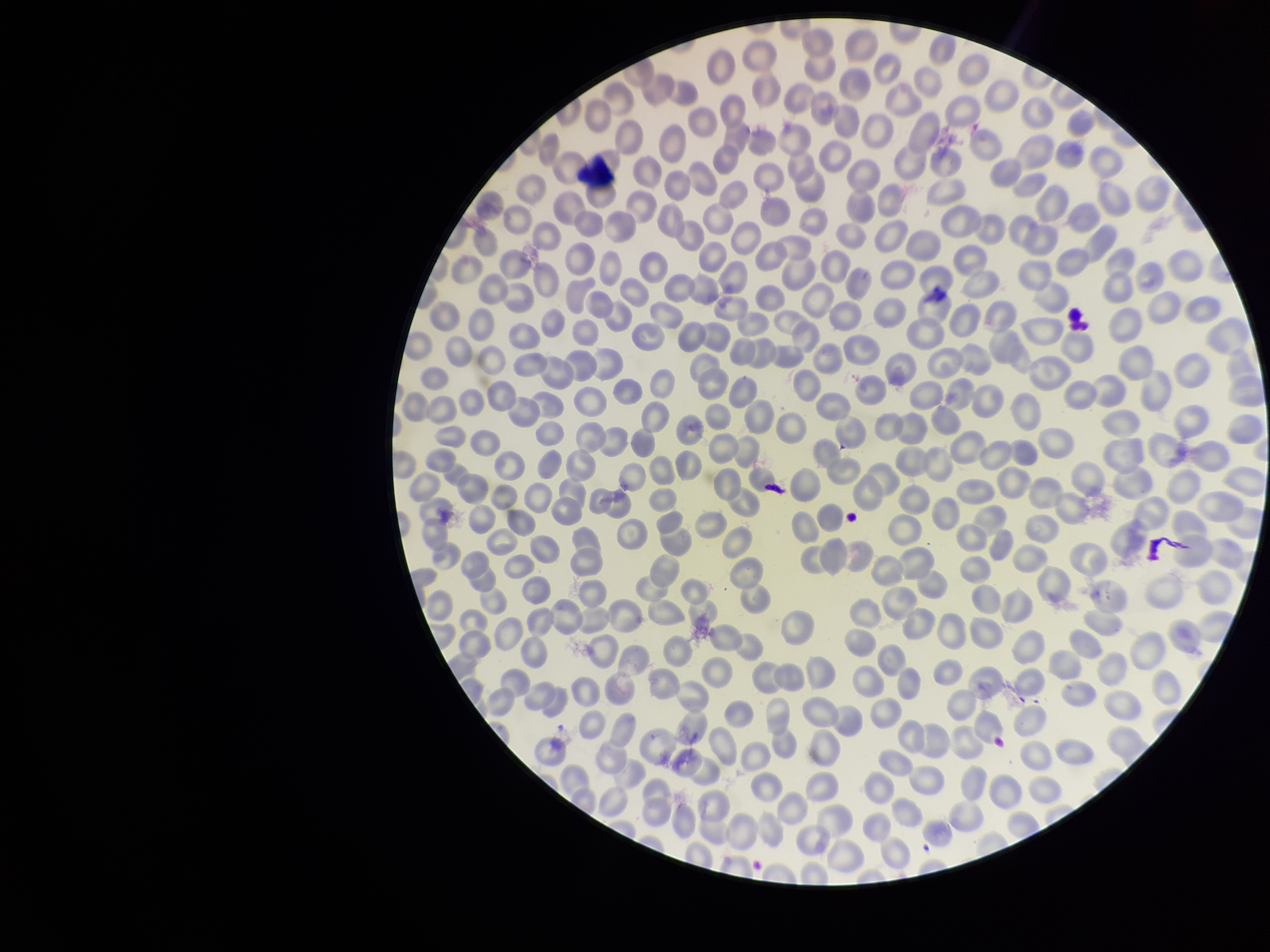

Patient malaria status: infected. Parasitized red blood cells: none seen. Image is 1270×952 pixels. Smartphone photograph taken through the eyepiece of a microscope. Preparation: thin blood smear. Red blood cell count: 341. Parasitized red blood cell count: 0. Single field of view. Species reported for this patient: Plasmodium falciparum. Giemsa stain.